Locate every blood parasite and identify its species.
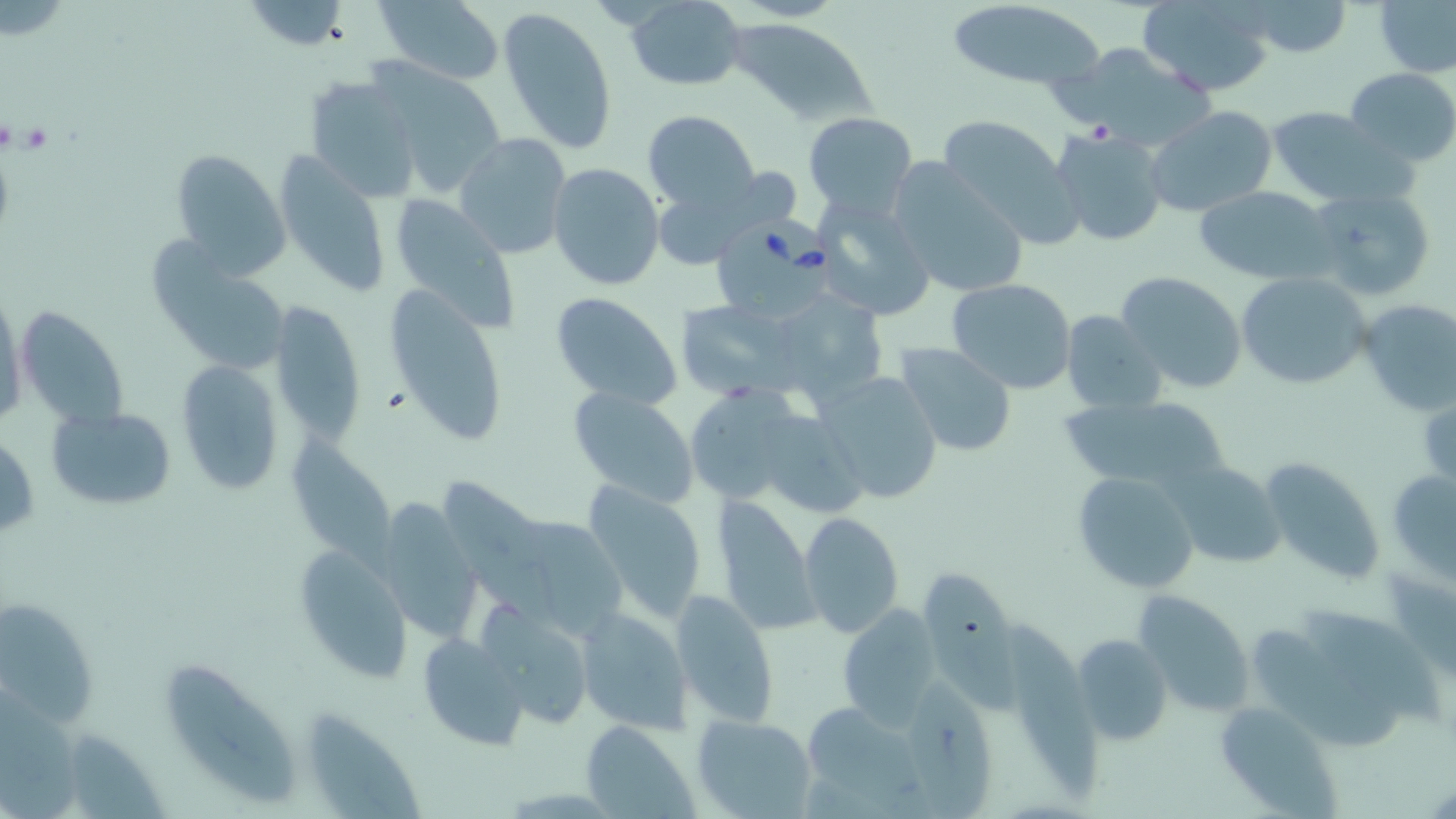
Approximate bounding boxes as [x1, y1, x2, y2] in pixels.
Babesia divergens-infected red blood cells: [715, 223, 830, 321].
No Plasmodium falciparum, Plasmodium ovale, Plasmodium malariae, Plasmodium vivax, or Trypanosoma brucei observed.

Summary:
  - Platelet locations: [16, 121, 53, 155], [381, 384, 412, 415]
  - Uninfected red blood cell locations: [625, 0, 746, 91], [945, 0, 1104, 90], [1138, 0, 1276, 96], [243, 1, 350, 49], [372, 1, 507, 85], [1244, 1, 1352, 57], [1374, 1, 1456, 77], [498, 6, 617, 155], [728, 18, 879, 128], [378, 63, 506, 194], [1345, 68, 1456, 166], [304, 75, 423, 201], [1144, 106, 1279, 218], [1262, 106, 1402, 204], [642, 109, 759, 213], [803, 112, 917, 216], [936, 114, 1083, 245], [1050, 128, 1170, 247], [454, 132, 571, 260], [169, 148, 288, 276], [275, 151, 392, 296], [884, 160, 1030, 300], [548, 163, 667, 293], [657, 167, 793, 266], [1193, 185, 1337, 285], [1307, 187, 1434, 301], [385, 193, 519, 327], [815, 196, 937, 320], [146, 229, 286, 372], [1115, 270, 1248, 394], [1235, 272, 1371, 390], [945, 277, 1077, 393], [386, 283, 507, 450], [1, 290, 27, 429], [549, 291, 683, 410], [775, 293, 887, 401], [273, 298, 364, 452], [1357, 298, 1455, 415], [678, 299, 807, 401], [18, 305, 133, 432], [1062, 309, 1166, 414], [896, 341, 1017, 456], [176, 362, 283, 495], [816, 371, 943, 504], [681, 381, 811, 509], [568, 385, 699, 508], [1058, 395, 1233, 498], [47, 404, 178, 511], [766, 419, 869, 514], [286, 425, 401, 577], [0, 431, 39, 543], [1256, 456, 1386, 586], [1166, 462, 1286, 568], [1387, 465, 1456, 582], [1070, 470, 1202, 594], [436, 477, 553, 617], [583, 480, 707, 624], [717, 495, 820, 633], [374, 500, 480, 641], [798, 511, 905, 638], [519, 514, 637, 648], [293, 547, 412, 683], [928, 566, 1024, 727], [670, 590, 781, 728], [1132, 590, 1253, 717], [0, 593, 100, 731], [834, 604, 944, 727], [483, 606, 596, 732], [1301, 606, 1440, 725], [575, 608, 693, 734], [1003, 615, 1105, 803], [1255, 620, 1402, 751], [419, 633, 529, 747], [1070, 633, 1174, 746], [158, 655, 302, 805], [911, 677, 992, 819], [1213, 700, 1345, 817], [794, 701, 931, 813], [308, 703, 427, 815], [692, 714, 817, 818], [580, 720, 698, 817], [67, 728, 170, 816]
  - Slide-level diagnosis: Babesia divergens
  - Preparation: thin blood smear
  - Image size: 1456×819 pixels
  - Modality: light microscopy
  - Stain: May-Grünwald-Giemsa
  - Magnification: 1000x
  - Field of view: one of a larger specimen